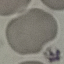
result = no malaria parasites seen
image type = automatically extracted cell patch, resized to 64 × 64 pixels
capture = smartphone camera at the microscope eyepiece
stain = Giemsa
preparation = thin blood film